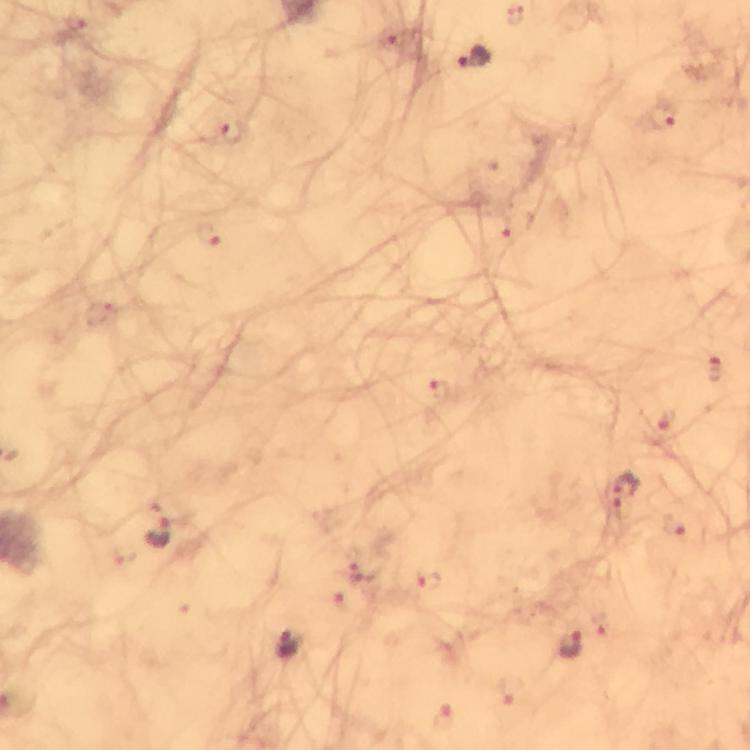
Approximate centers as {x, y} in pixels.
Summary:
  - Plasmodium parasite locations: {475, 59}, {663, 119}, {232, 132}, {718, 372}, {625, 490}, {157, 525}, {429, 580}, {290, 644}, {573, 645}
  - Preparation: thick blood film
  - Immersion oil: applied
  - Cropped from: a single field of view
  - Stain: Giemsa
  - Magnification: 100x
  - Context: from a diagnostic examination for malaria
  - Image size: 750×750 pixels
  - Capture: smartphone photograph through a microscope